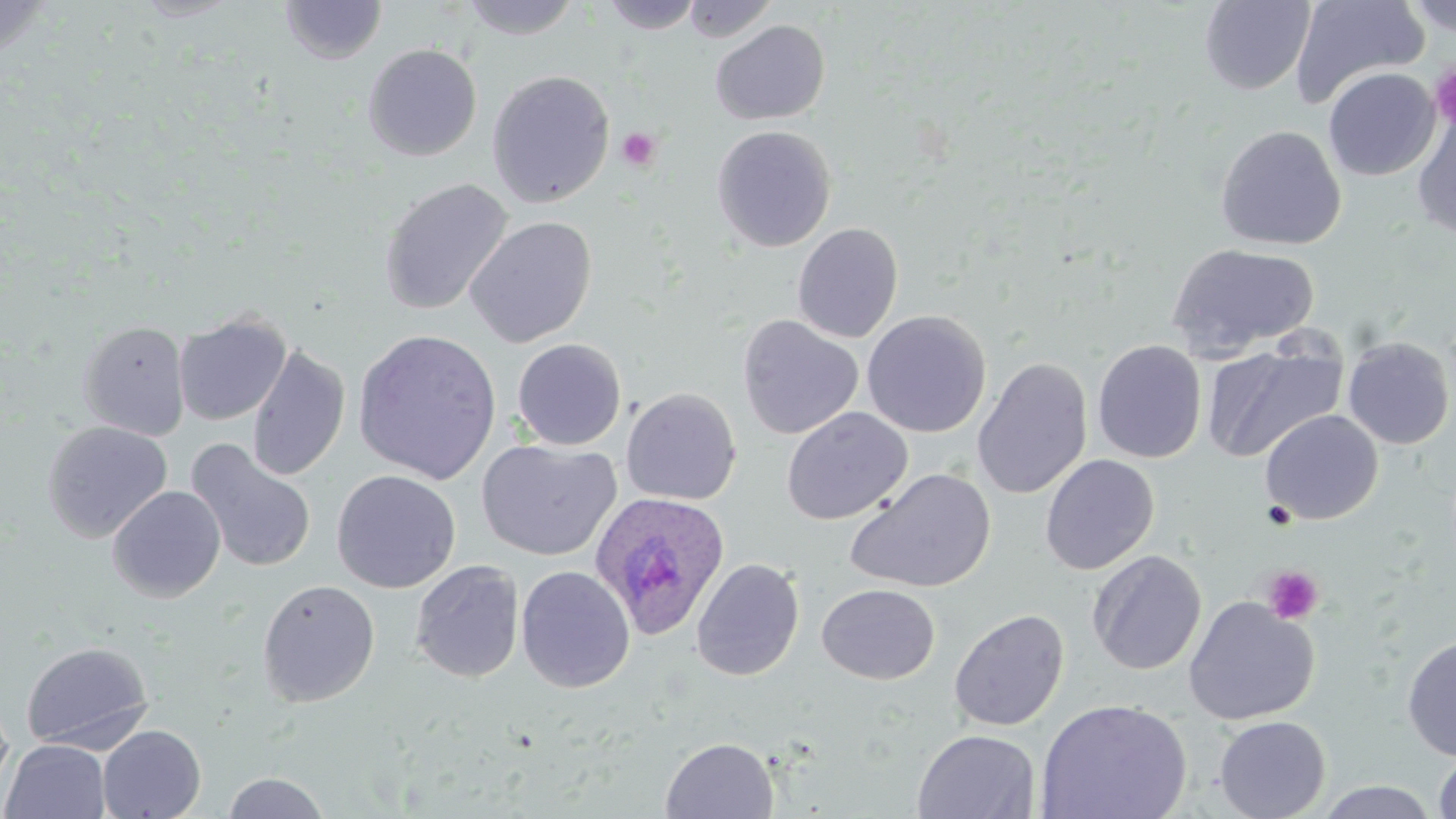

Approximate bounding boxes as (x1,y1)-(x2,y2) corner pairs in pixels. Plasmodium ovale-infected red blood cell locations: (590,492)-(731,640). Platelet locations: (1430,64)-(1456,129), (616,127)-(661,171), (1262,565)-(1324,625). Uninfected red blood cell locations: (1,0)-(53,61), (131,0)-(244,22), (459,0)-(583,39), (682,0)-(779,42), (1289,0)-(1430,110), (1404,0)-(1454,37), (279,1)-(387,64), (601,1)-(701,34), (1199,1)-(1316,95), (710,20)-(830,125), (362,43)-(482,161), (1323,67)-(1440,181), (486,70)-(615,208), (1412,108)-(1456,239), (712,125)-(836,252), (1215,125)-(1346,250), (378,177)-(513,316), (464,215)-(597,348), (792,222)-(904,343), (1167,242)-(1319,357), (862,310)-(991,438), (173,312)-(291,426), (737,315)-(863,440), (78,320)-(190,440), (353,328)-(503,485), (1342,336)-(1455,449), (511,338)-(627,451), (1092,339)-(1207,463), (1201,340)-(1347,463), (246,344)-(350,482), (793,353)-(942,490), (973,357)-(1093,500), (621,387)-(741,505), (782,406)-(912,525), (1260,409)-(1383,525), (42,421)-(172,543), (185,438)-(318,574), (476,438)-(622,561), (1040,454)-(1159,575), (845,467)-(996,594), (331,469)-(461,594), (107,485)-(226,603), (1088,550)-(1207,676), (691,558)-(805,681), (410,560)-(525,682), (516,565)-(635,693), (257,579)-(380,707), (817,583)-(940,684), (1182,596)-(1320,725), (948,608)-(1070,732), (1401,634)-(1456,762), (21,641)-(153,753), (0,691)-(14,806), (1035,698)-(1193,819), (1213,715)-(1331,819), (97,725)-(206,819), (913,729)-(1040,818), (661,737)-(779,818), (2,739)-(111,819), (1432,747)-(1456,818), (222,772)-(331,818), (1313,780)-(1442,818). Slide-level diagnosis: Plasmodium ovale. Captured at 1000x magnification. Image is 1456×819 pixels. May-Grünwald-Giemsa stain. Light microscopy. Single field of view. Thin blood smear.